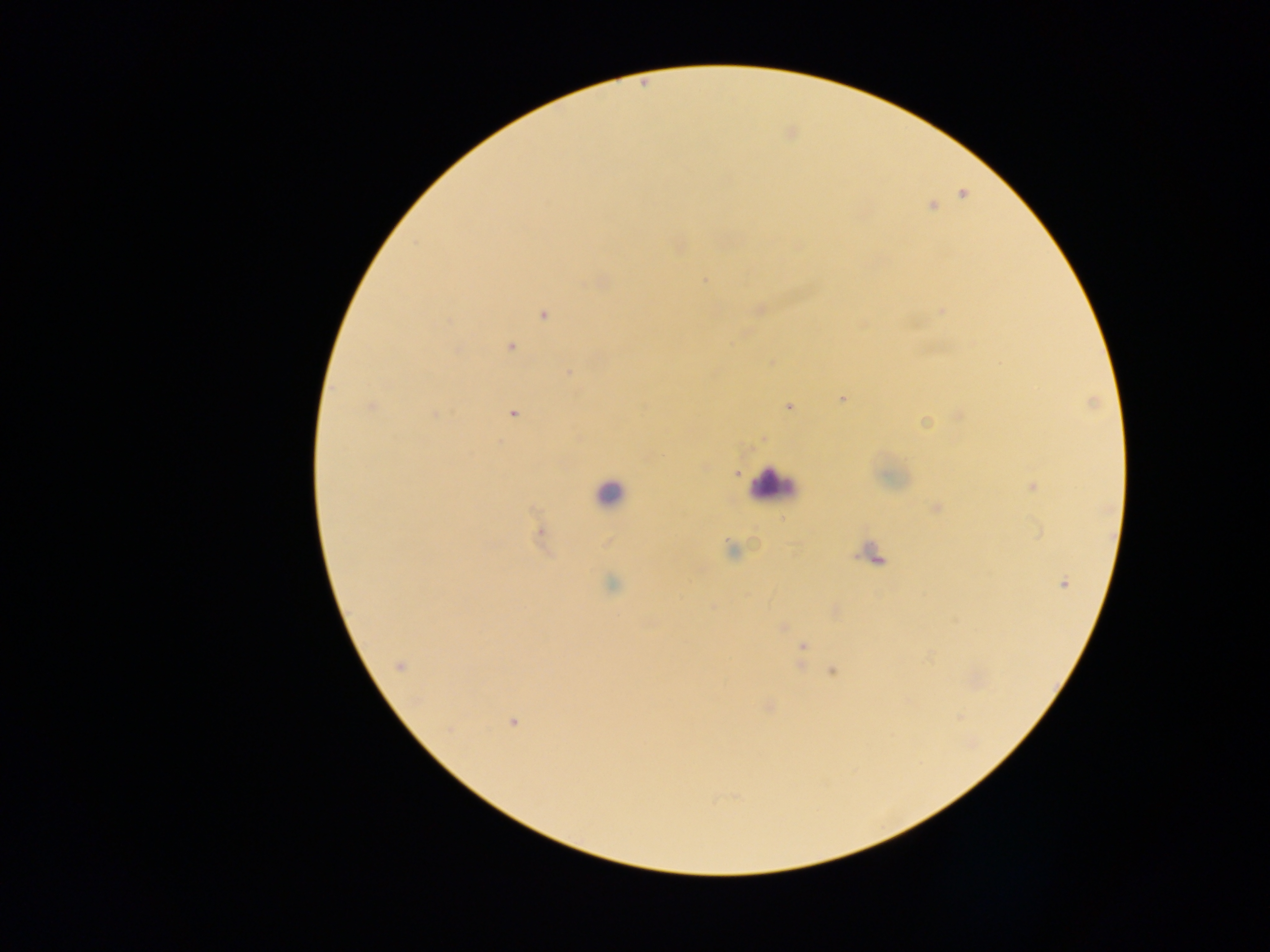
image size = 1270×952 pixels
capture = mobile-phone photograph through a microscope
leukocyte locations = approximate centers as (x, y) in pixels: (773, 486), (608, 493)
Plasmodium parasite locations = approximate centers as (x, y) in pixels: (963, 193), (931, 206), (678, 246), (797, 246), (599, 280), (703, 280), (759, 309), (942, 311), (544, 313), (511, 346), (771, 361), (568, 372), (843, 398), (371, 406), (788, 406), (513, 413), (435, 415), (959, 415), (924, 423), (763, 438), (704, 467), (735, 473), (1032, 485), (935, 508), (540, 533), (730, 551), (1063, 582), (612, 585), (835, 611), (782, 627), (802, 647), (400, 666), (831, 670), (768, 706), (513, 722)
preparation = thick blood smear
field of view = single
country = Ghana